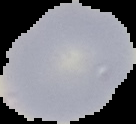

Summary:
  - Preparation: thin blood film
  - Malaria status: uninfected
  - Image size: 136×124 pixels
  - Image type: cell region segmented out of the field of view; surrounding area masked to black